Point out each Plasmodium parasite.
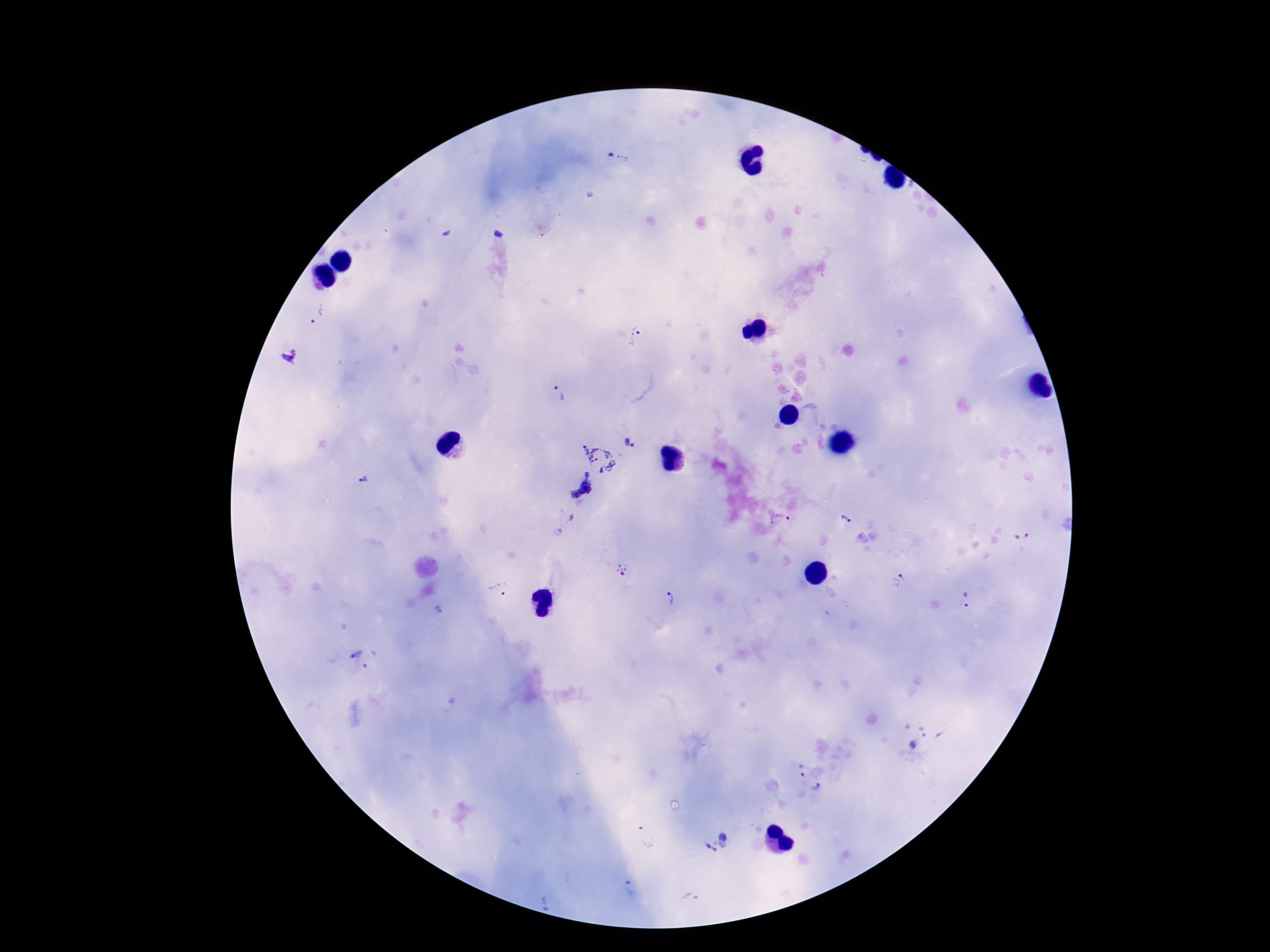

Approximate centers as (x, y) in pixels.
Plasmodium parasites: (619, 157), (499, 233), (318, 315), (636, 335), (290, 355), (561, 394), (631, 443), (599, 457), (363, 480), (582, 490), (847, 520), (780, 521), (563, 522), (1024, 536), (623, 569), (899, 580), (499, 589), (669, 597), (964, 600), (439, 610), (357, 661), (922, 731), (912, 745), (801, 770), (816, 788), (645, 836), (717, 842), (629, 890), (691, 898), (546, 902).

image size = 1270×952 pixels
capture = smartphone camera through the microscope eyepiece
preparation = thick peripheral-blood smear
stain = Giemsa
field of view = one from this slide
patient malaria status = positive
magnification = 100x